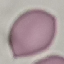

Summary:
  - Malaria status: uninfected
  - Preparation: thin blood smear
  - Stain: Giemsa
  - Image type: cell patch, automatically extracted from a larger field of view and resized to 64 × 64 pixels
  - Capture: smartphone through the microscope eyepiece